Report the malaria status.
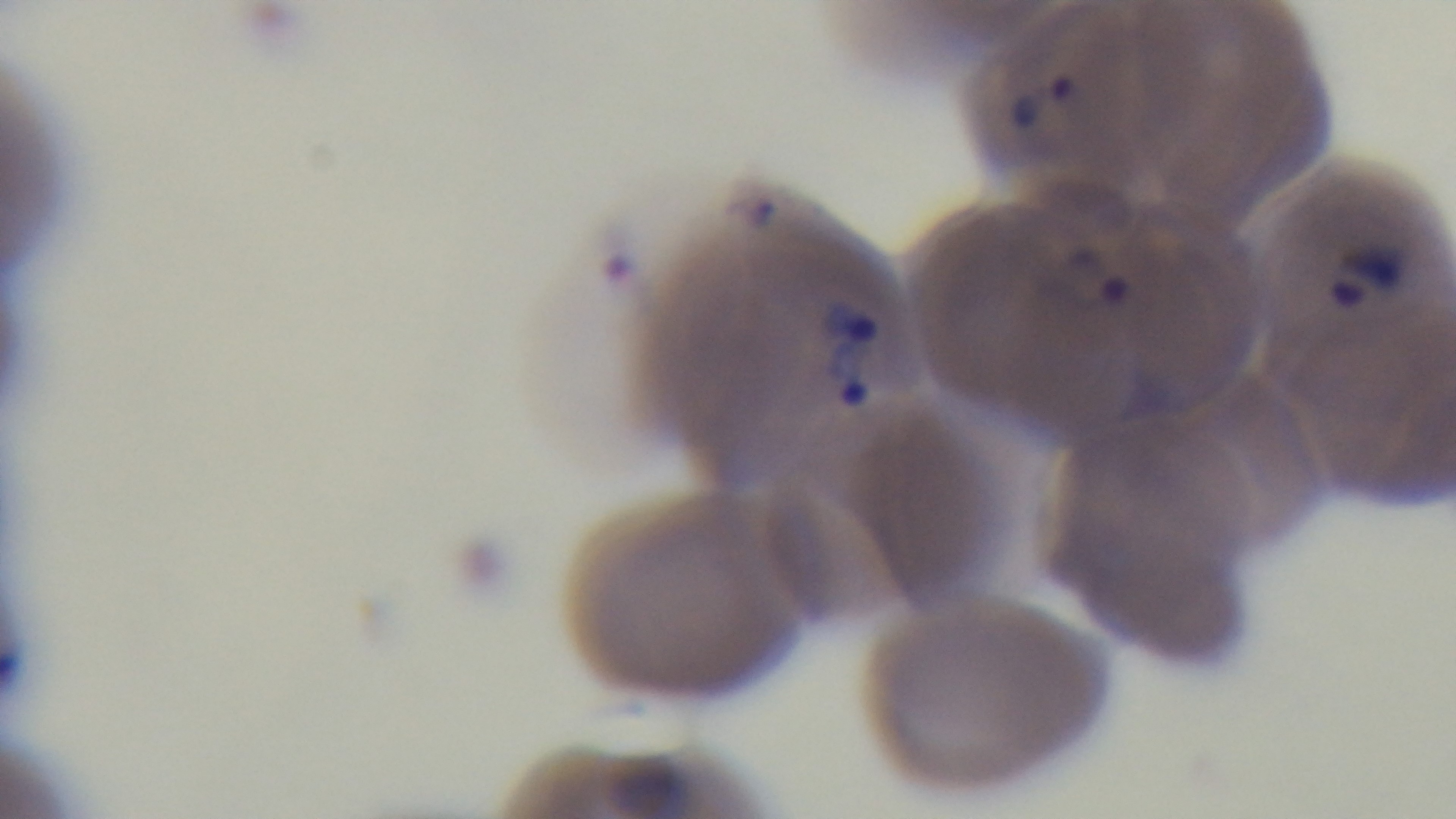
It is infected.

Summary:
  - Preparation: thin blood film
  - Field of view: one from the slide
  - Modality: light microscopy
  - Objective: 100x oil immersion
  - Capture: mounted 4K digital camera
  - Stain: Giemsa